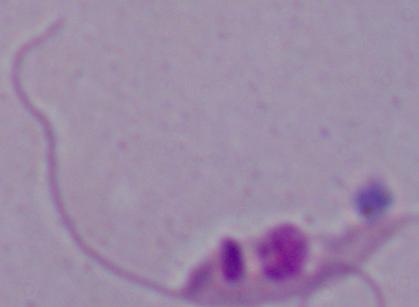

Micrograph. Captured at 1000x magnification. A Leishmania parasite is shown.